Classify this cell by malaria status.
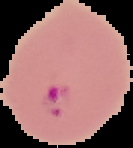

It is parasitized.

Segmented cell region on a black background. Image is 133×148 pixels. From a thin blood smear.